Assess this cell for malaria.
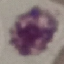

It is uninfected.

capture: smartphone camera at the microscope eyepiece
stain: Giemsa
preparation: thin smear
image_type: cell patch, automatically extracted from a larger field of view and resized to 64 × 64 pixels